Name the cell type shown.
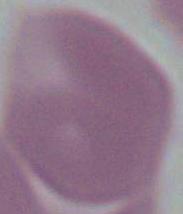
An erythrocyte.

Photomicrograph. Captured at 1000x magnification.